Describe the morphology of the erythrocytes.
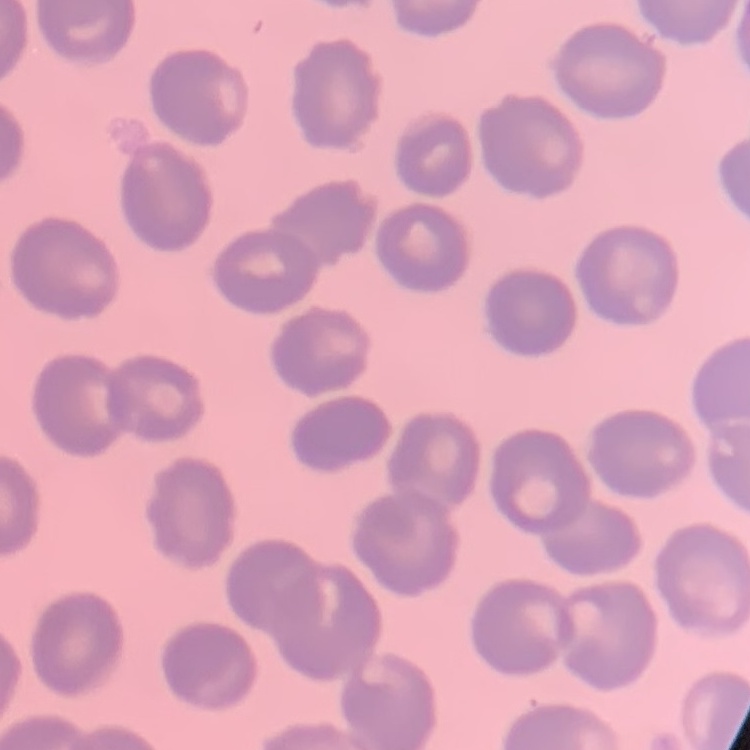

They show no rouleaux formation.

One tile cut from a larger photomicrograph. Thin peripheral smear. Field's or Giemsa stain.